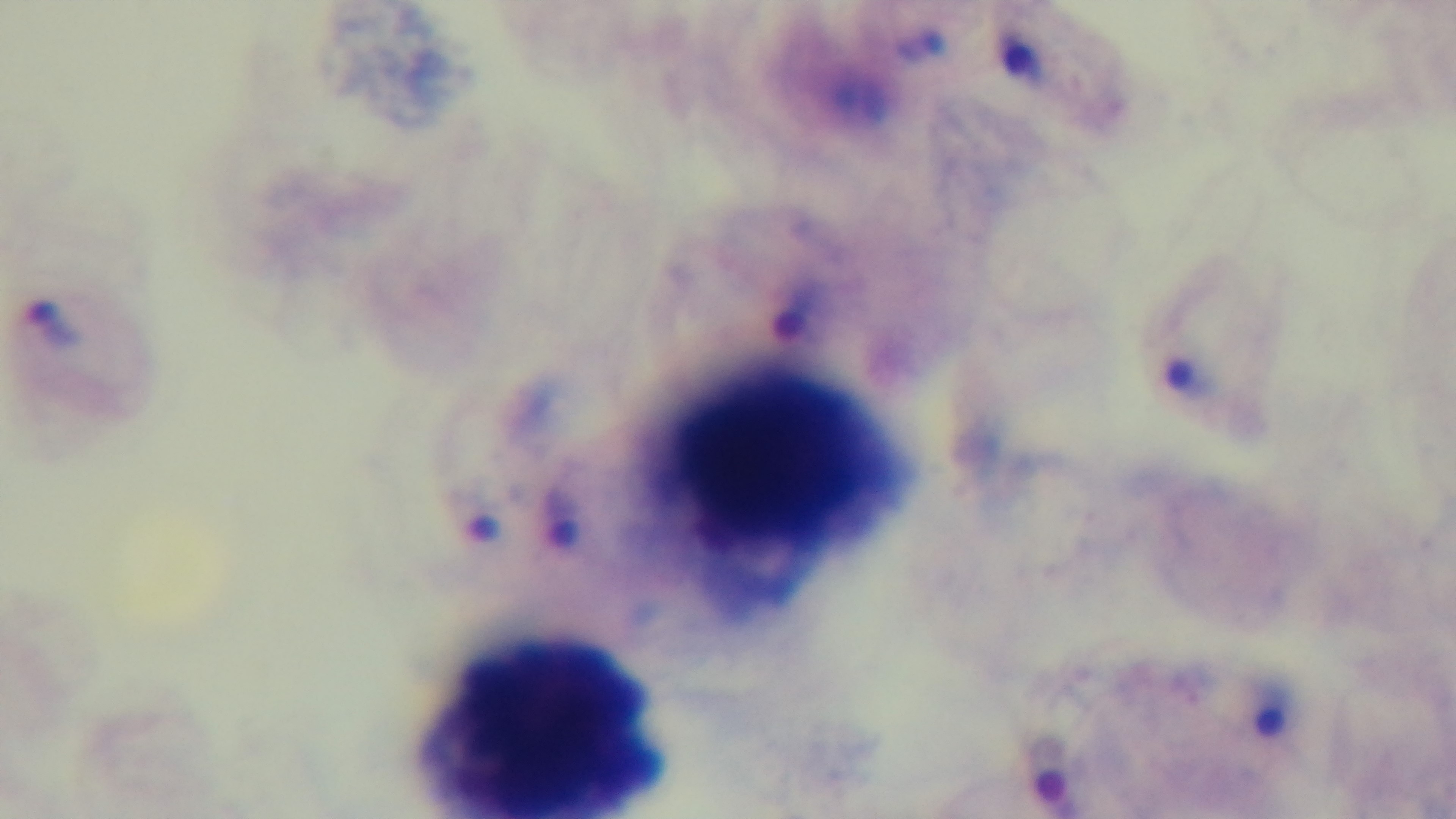

field of view = single
malaria status = positive
modality = light microscopy
preparation = thick
capture = mounted 4K digital camera
stain = Giemsa
objective = 100x oil immersion